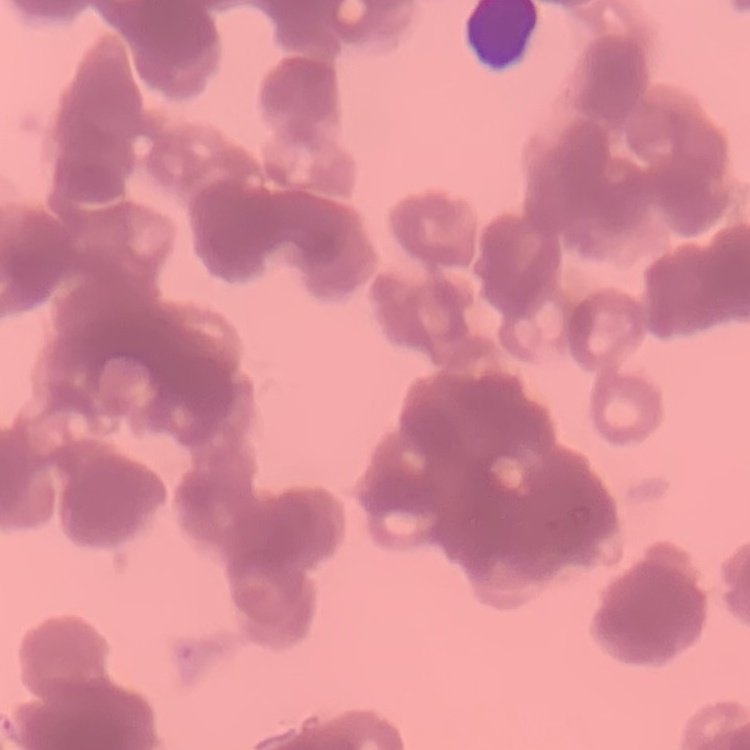

Summary:
  - Erythrocyte morphology: rouleaux formation
  - Stain: Field's or Giemsa
  - Image type: square crop of a larger photomicrograph
  - Preparation: thin blood film